Outline each blood parasite and name the species.
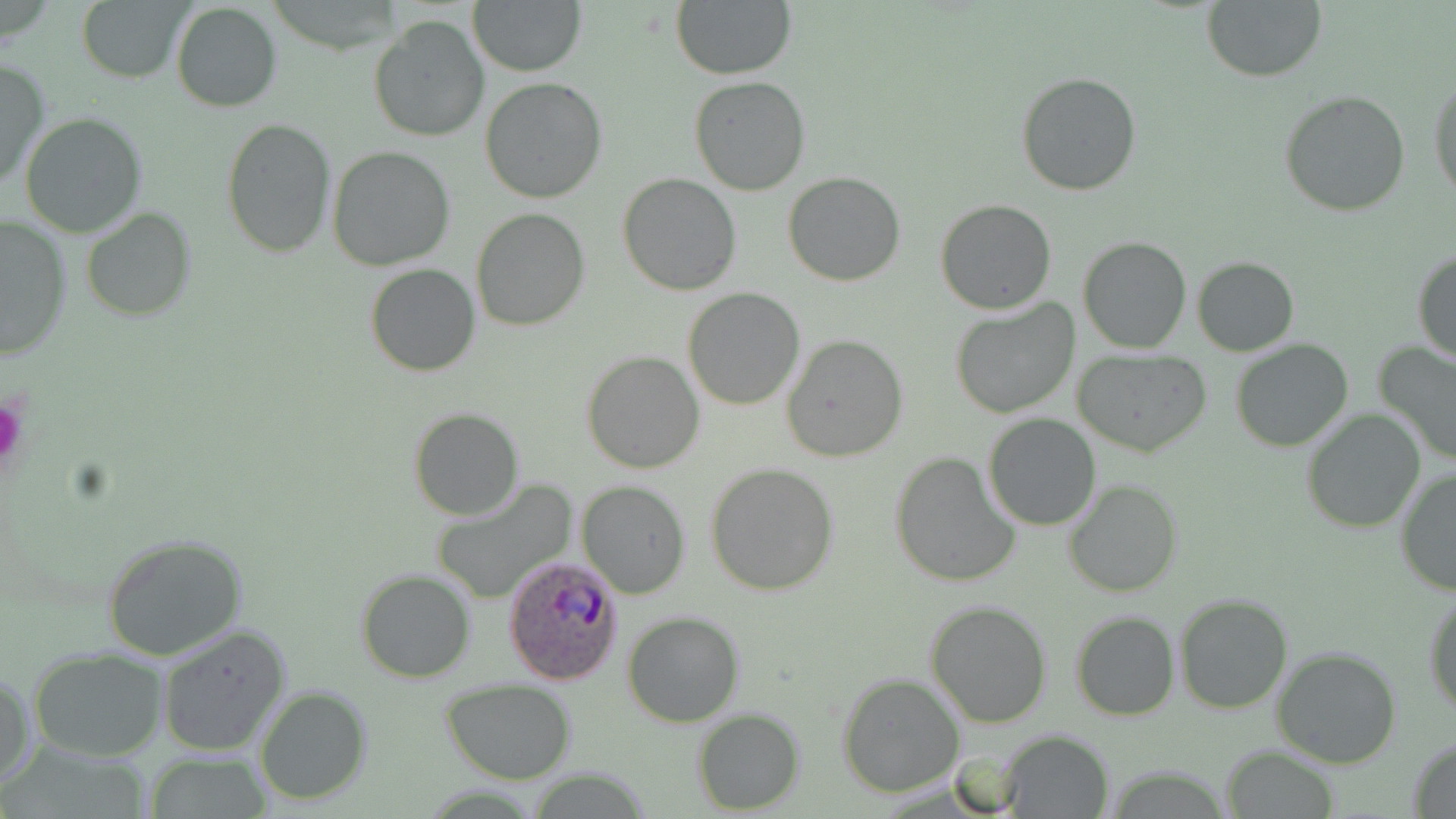
Approximate bounding boxes as (x1,y1)-(x2,y2) corner pairs in pixels.
Plasmodium ovale-infected red blood cells: (502,553)-(625,686).
No Plasmodium falciparum, Plasmodium malariae, Plasmodium vivax, Babesia divergens, or Trypanosoma brucei observed.

slide_level_diagnosis: Plasmodium ovale
modality: light microscopy
platelet_locations: 'approximate bounding boxes as (x1,y1)-(x2,y2) corner pairs in pixels: (0,394)-(25,474)'
image_size: 1456×819 pixels
stain: May-Grünwald-Giemsa
field_of_view: one of a larger specimen
uninfected_red_blood_cell_locations: 'approximate bounding boxes as (x1,y1)-(x2,y2) corner pairs in pixels: (467,0)-(586,76), (1201,0)-(1326,82), (671,1)-(795,79), (77,2)-(187,83), (170,2)-(282,114), (368,15)-(489,142), (0,60)-(49,191), (1016,71)-(1142,195), (1429,73)-(1456,204), (689,76)-(810,195), (480,78)-(607,205), (1279,89)-(1411,216), (19,112)-(148,238), (221,118)-(335,258), (328,145)-(456,270), (618,172)-(741,295), (784,172)-(906,287), (936,199)-(1056,315), (471,207)-(592,331), (80,209)-(195,323), (0,215)-(72,358), (1078,236)-(1191,352), (1413,249)-(1455,365), (1191,256)-(1299,355), (365,263)-(480,377), (683,287)-(804,410), (949,298)-(1081,420), (781,335)-(908,461), (1231,340)-(1355,452), (1375,341)-(1456,466), (582,351)-(705,474), (1074,351)-(1211,457), (408,407)-(524,520), (1301,409)-(1426,533), (981,412)-(1103,531), (890,450)-(1023,588), (706,462)-(840,595), (1395,470)-(1455,596), (1063,480)-(1182,598), (431,481)-(577,605), (577,481)-(691,599), (98,531)-(249,663), (355,570)-(476,683), (1424,588)-(1456,716), (1173,593)-(1293,715), (925,598)-(1053,728), (1070,610)-(1179,721), (622,611)-(745,728), (156,623)-(291,755), (1273,646)-(1401,768), (28,648)-(166,762), (1,669)-(35,793), (836,671)-(965,797), (441,680)-(577,783), (255,684)-(374,806), (692,709)-(806,814), (993,729)-(1115,816), (1407,735)-(1456,818), (1221,744)-(1339,819), (144,755)-(275,817)'
magnification: 1000x
preparation: thin blood smear